Give a bounding box for every trophozoite.
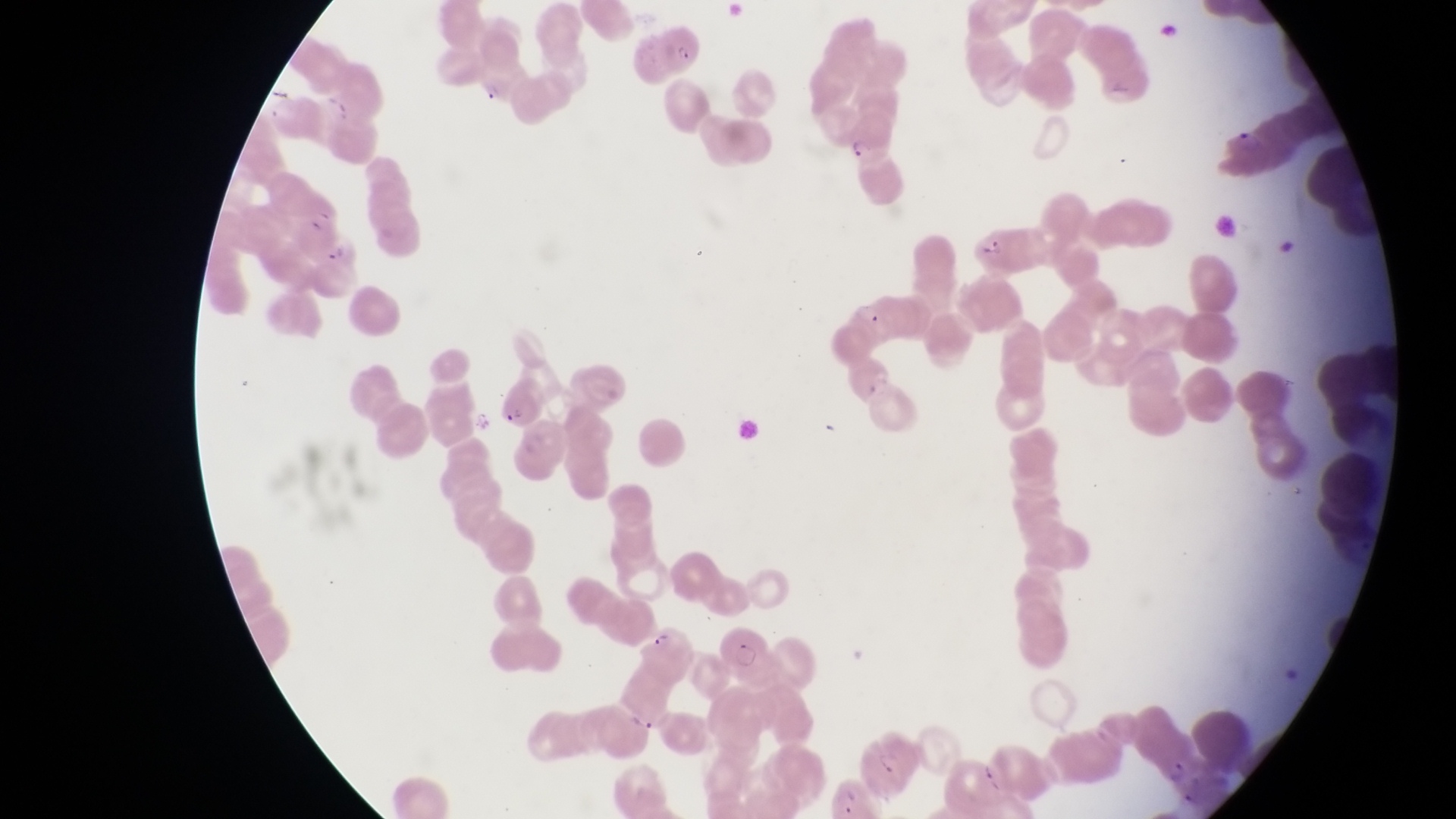
Approximate bounding boxes as {left, top, right, bottom} in pixels.
Trophozoites: {479, 85, 503, 108}, {851, 139, 877, 162}, {855, 300, 881, 329}.

Parasitised red blood cell locations: {661, 19, 710, 75}, {1212, 119, 1270, 177}, {964, 221, 1033, 273}, {311, 227, 358, 274}, {491, 384, 543, 427}, {640, 620, 699, 686}, {714, 620, 766, 667}, {851, 737, 920, 798}. Image is 1456×819 pixels. Photographed through the eyepiece of an Olympus CX-23 microscope with a smartphone camera. Thin blood smear. At a magnification of 1000x. One field of view. Collected in Uganda.